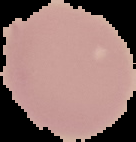

Summary:
  - Image size: 136×142 pixels
  - Image type: segmented cell region on a black background
  - Malaria status: uninfected
  - Preparation: thin blood smear